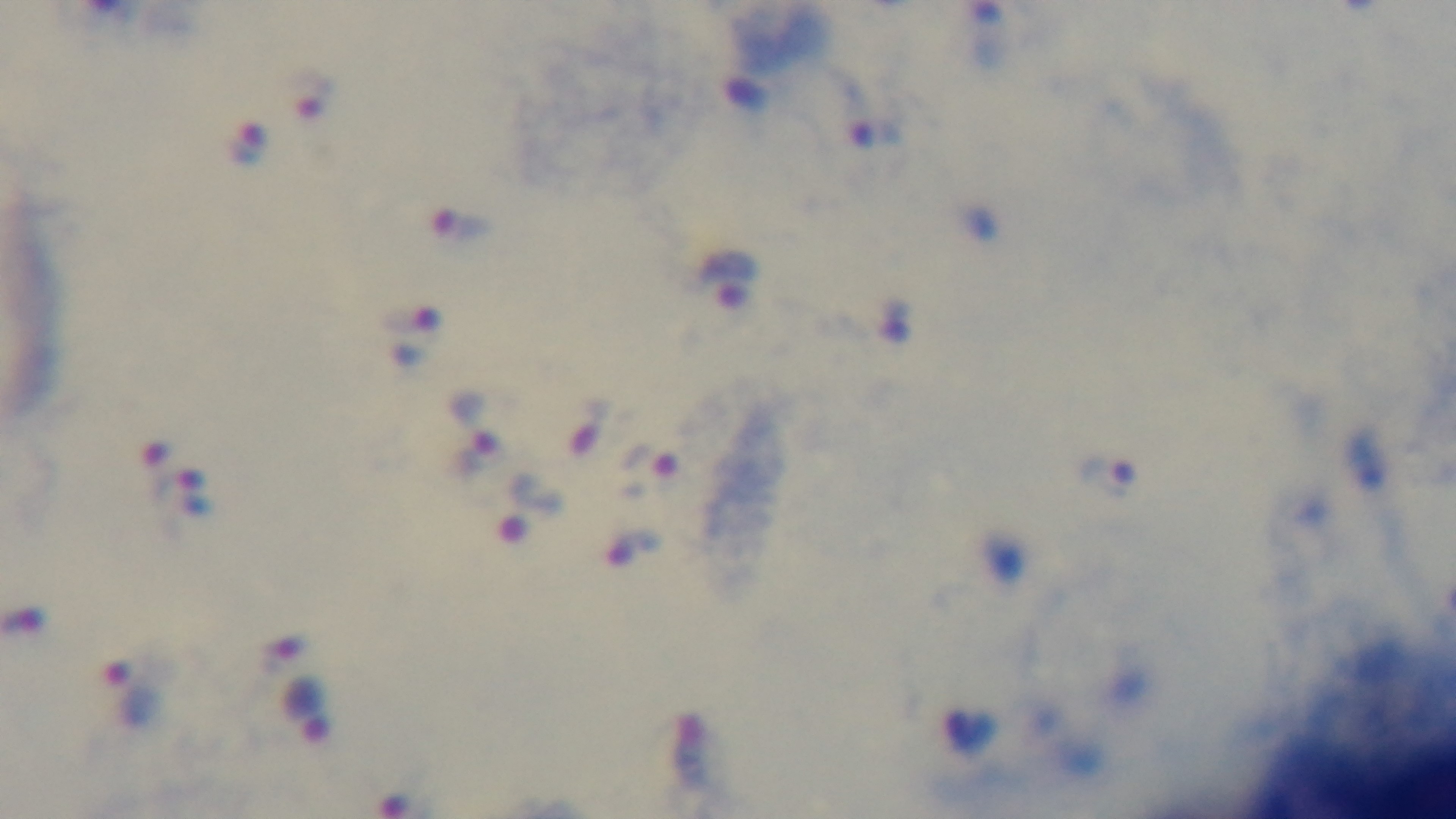

{
  "capture": "mounted 4K digital camera",
  "stain": "Giemsa",
  "objective": "100x oil immersion",
  "modality": "light microscopy",
  "preparation": "thick",
  "malaria_status": "positive",
  "field_of_view": "single"
}